Comment on the morphology of the red blood cells.
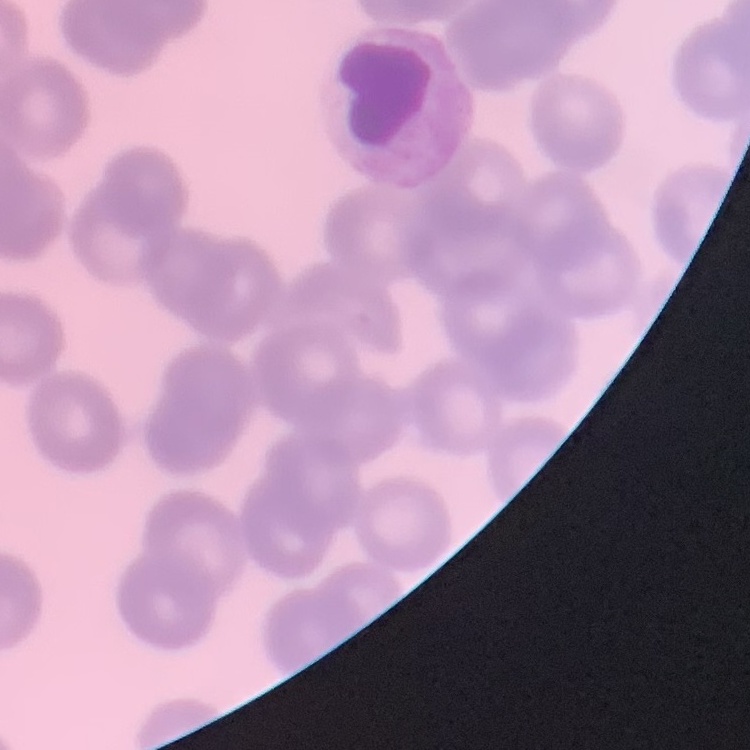

They show no rouleaux formation.

image type = one tile cut from a larger photomicrograph
stain = Field's or Giemsa
preparation = thin blood smear